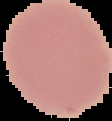

{
  "image_type": "cell region segmented out of the field of view; surrounding area masked to black",
  "preparation": "thin blood film",
  "image_size": "112×121 pixels",
  "malaria_status": "uninfected"
}